Assess the morphology of the red blood cells.
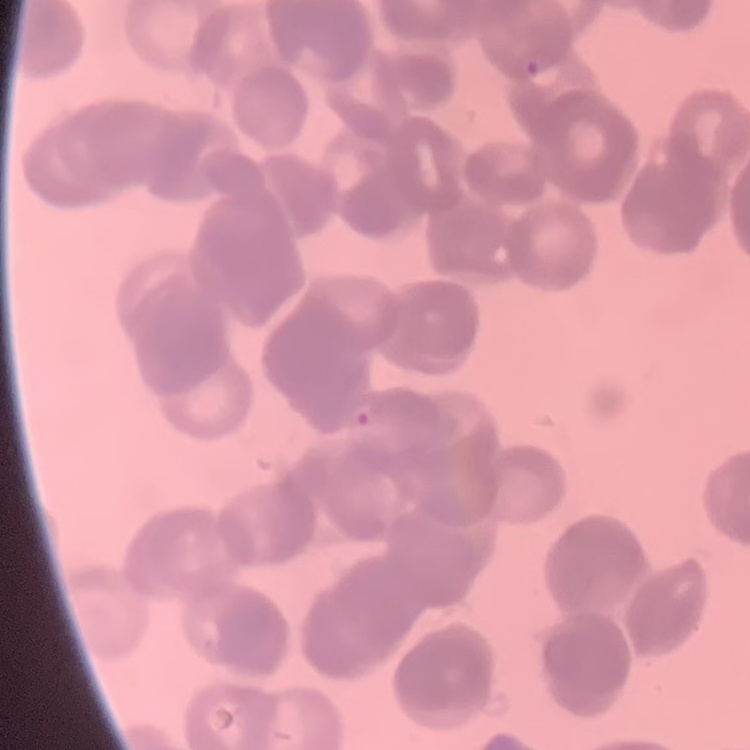

Rouleaux formation.

Summary:
  - Stain: Field's or Giemsa
  - Preparation: thin blood film
  - Image type: one tile cut from a larger photomicrograph